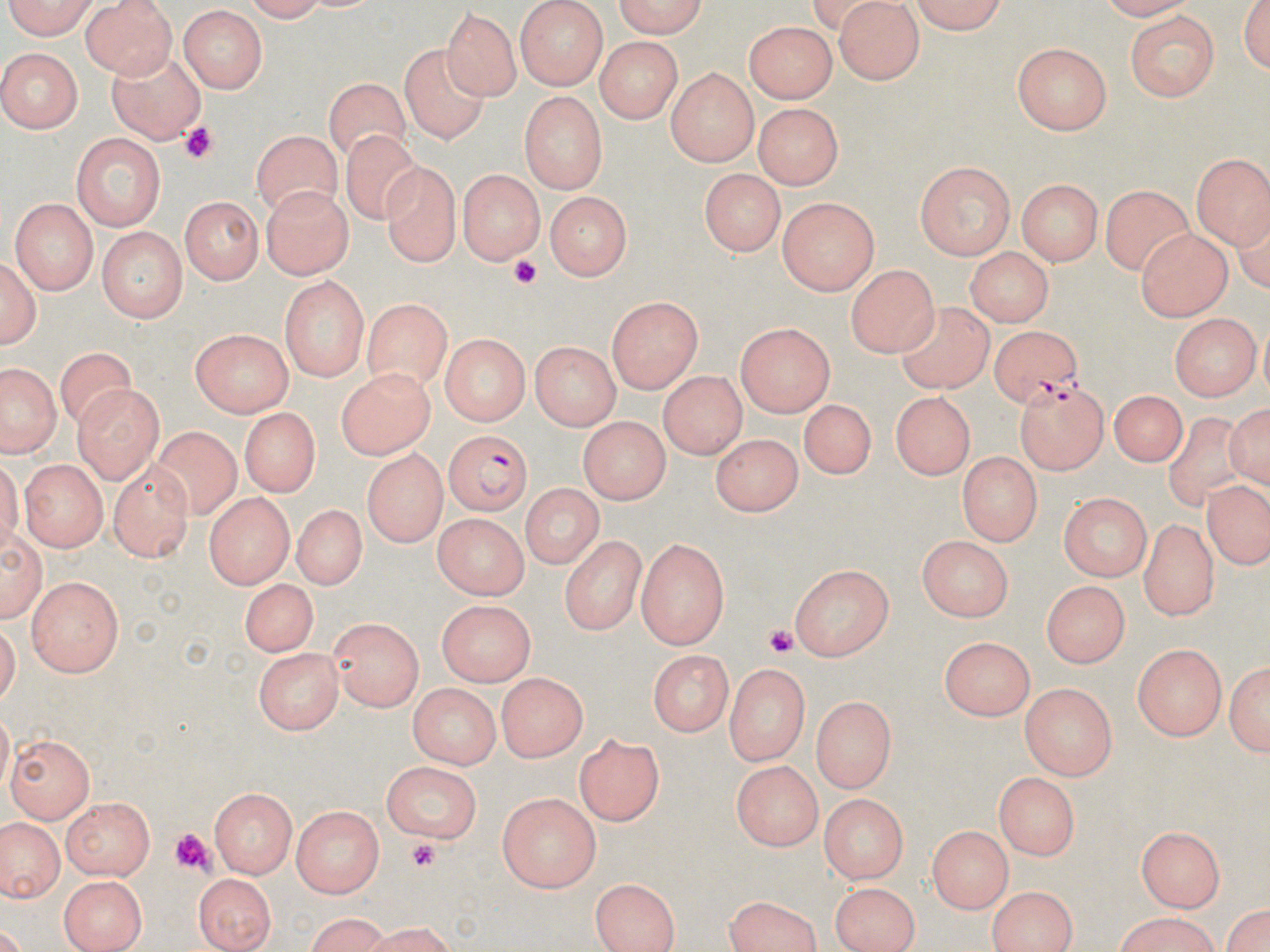

Summary:
  - Coordinate format: approximate bounding boxes as (x1,y1)-(x2,y2) corner pairs in pixels
  - Platelet locations: (175,125)-(217,163), (508,255)-(541,287), (762,625)-(798,661), (171,828)-(217,878), (406,838)-(438,872)
  - Plasmodium falciparum-infected red blood cell locations: (990,327)-(1083,403), (1016,382)-(1109,473), (444,432)-(531,517)
  - Uninfected red blood cell locations: (3,0)-(101,39), (80,0)-(179,77), (515,0)-(608,88), (605,0)-(708,35), (902,0)-(1012,32), (1236,0)-(1270,77), (833,1)-(923,82), (178,7)-(270,93), (443,7)-(518,102), (1125,11)-(1220,102), (744,18)-(840,102), (592,37)-(684,121), (1012,42)-(1113,135), (401,44)-(490,146), (106,46)-(202,145), (0,48)-(81,135), (666,68)-(760,167), (326,80)-(410,165), (517,90)-(607,192), (751,103)-(845,188), (338,125)-(425,225), (252,129)-(342,218), (71,131)-(166,228), (1192,152)-(1269,246), (377,157)-(459,264), (914,162)-(1016,259), (456,167)-(545,265), (699,170)-(782,257), (1019,178)-(1102,265), (1103,184)-(1194,272), (262,185)-(352,281), (546,194)-(632,278), (181,195)-(264,283), (10,198)-(96,293), (776,199)-(878,295), (97,227)-(188,322), (1135,227)-(1232,320), (962,245)-(1056,325), (1,254)-(40,352), (846,265)-(938,356), (280,277)-(368,383), (607,297)-(704,393), (363,298)-(452,390), (899,299)-(996,396), (1169,313)-(1257,400), (734,321)-(834,415), (189,328)-(295,418), (438,334)-(531,425), (531,342)-(619,428), (54,347)-(137,439), (1,360)-(60,460), (336,368)-(429,460), (658,371)-(748,457), (73,381)-(164,480), (1107,387)-(1189,466), (894,390)-(975,476), (804,397)-(875,473), (1228,398)-(1270,493), (238,408)-(319,497), (1167,412)-(1251,511), (577,417)-(671,501), (153,424)-(244,516), (714,430)-(802,513), (360,449)-(446,547), (959,451)-(1043,545), (19,458)-(109,552), (108,459)-(195,561), (519,482)-(607,568), (1202,484)-(1270,572), (202,491)-(297,584), (1060,491)-(1151,580), (292,503)-(361,590), (430,513)-(530,597), (1141,518)-(1220,619), (562,533)-(645,636), (919,535)-(1013,622), (635,538)-(732,648), (788,562)-(896,663), (25,575)-(121,674), (239,578)-(319,655), (1040,581)-(1126,668), (436,602)-(533,683), (330,617)-(426,709), (938,636)-(1037,720), (1135,643)-(1226,740), (255,645)-(341,732), (646,649)-(734,739), (1226,657)-(1269,759), (722,663)-(811,764), (496,673)-(587,762), (1018,682)-(1120,776), (408,684)-(499,767), (812,697)-(894,795), (576,732)-(665,826), (9,735)-(95,819), (379,763)-(480,842), (734,763)-(820,852), (995,772)-(1081,856), (211,786)-(298,876), (493,792)-(602,890), (818,795)-(911,880), (62,797)-(156,880), (293,806)-(385,895), (2,814)-(63,903), (929,826)-(1012,910), (1135,826)-(1227,908), (58,871)-(146,952), (195,874)-(273,952), (591,877)-(682,951), (831,880)-(920,950), (988,885)-(1077,952), (1221,895)-(1270,952), (719,896)-(825,952), (296,914)-(393,951), (1108,915)-(1227,951)
  - Slide-level diagnosis: Plasmodium falciparum
  - Field of view: one of a larger specimen
  - Magnification: 1000x
  - Image size: 1270×952 pixels
  - Preparation: thin blood smear
  - Modality: optical microscopy
  - Stain: May-Grünwald-Giemsa